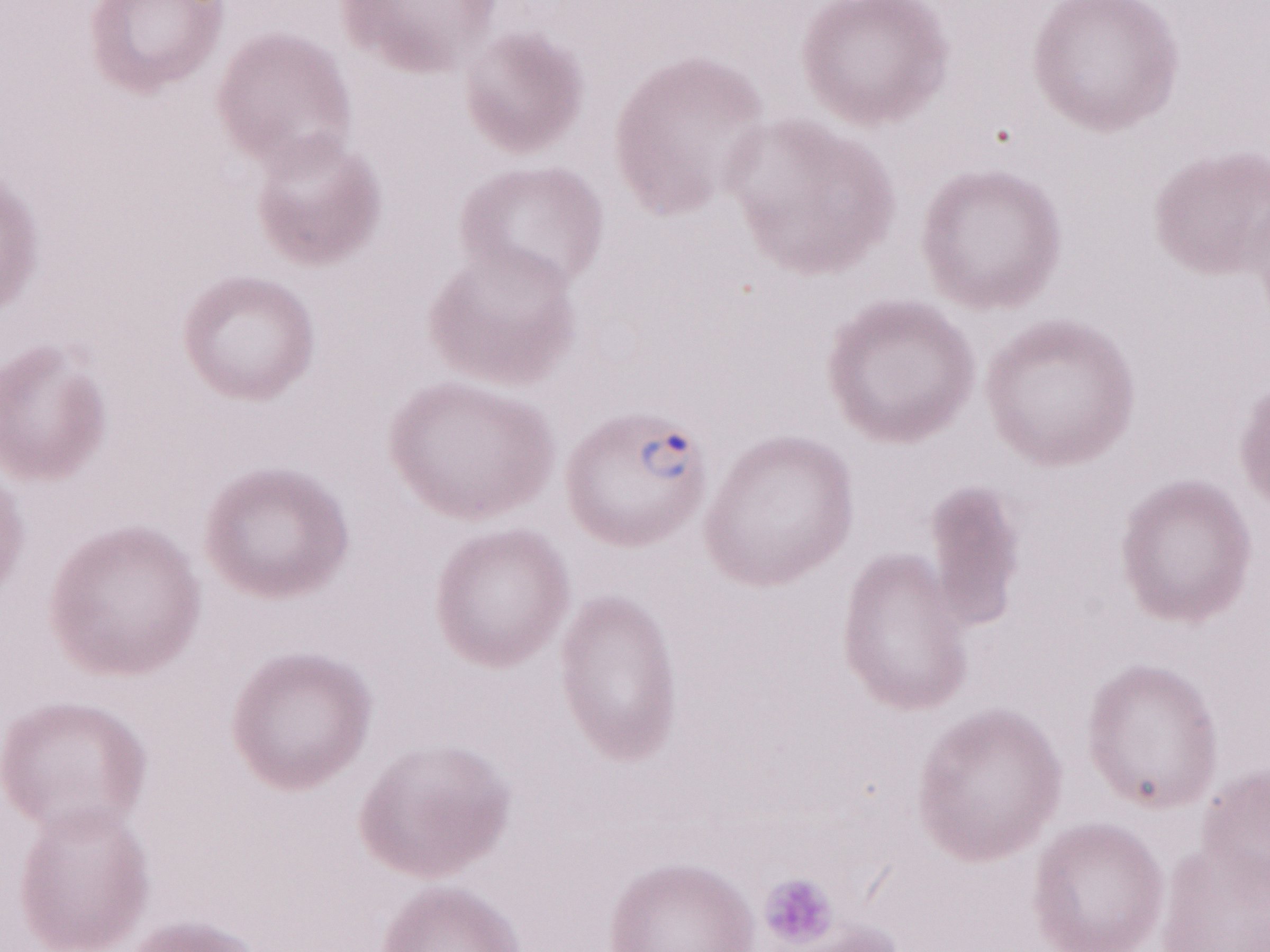 May-Grünwald-Giemsa (MGG) stain. One field of this slide. Image is 1270×952 pixels. Olympus BX43 microscope and DP73 digital camera. 1,000x magnification. Thin blood smear. Malaria diagnosis (patient-level): positive.